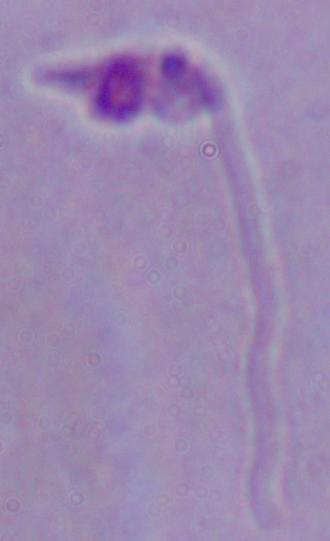
{
  "identification": "Leishmania",
  "magnification": "1000x",
  "modality": "photomicrograph"
}